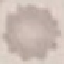 Result: no malaria parasites detected. Giemsa stain. Photographed with a smartphone camera at the microscope eyepiece. Thin smear of blood. Automatically extracted cell patch, resized to 64 × 64 pixels.